Identify the parasite.
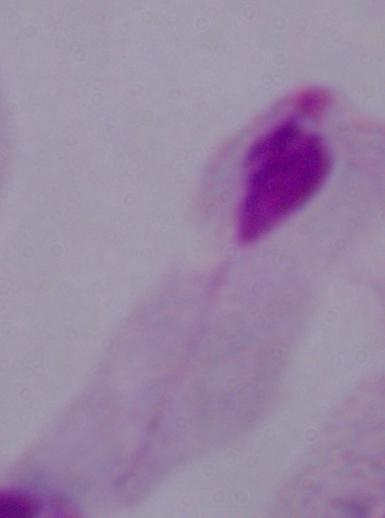

This is a trichomonad.

Summary:
  - Modality: photomicrograph
  - Magnification: 1000x